Classify this cell by malaria status.
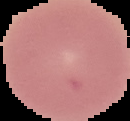

It is uninfected.

From a thin blood film. Image is 130×121 pixels. The area outside the segmented cell region is set to black.